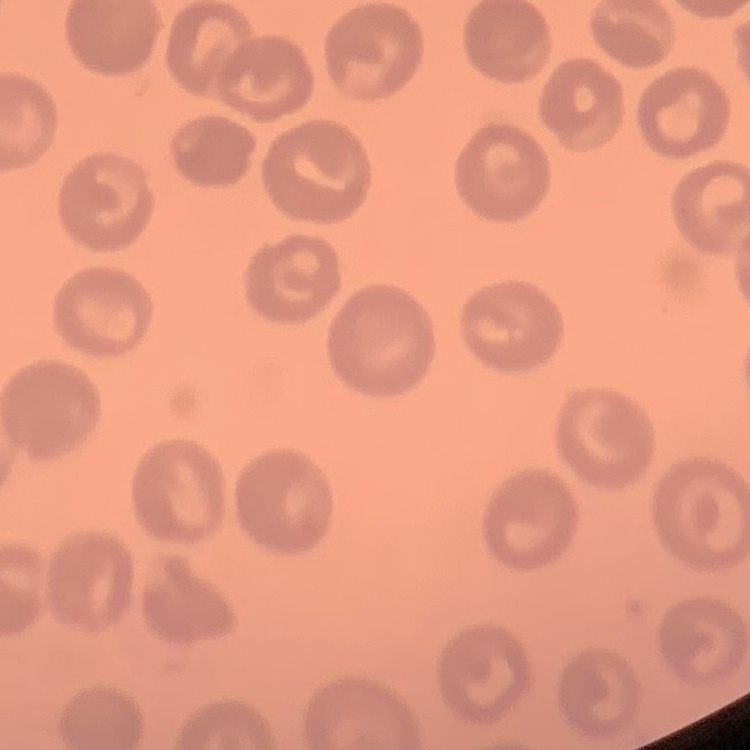
erythrocyte morphology = no rouleaux formation
preparation = thin blood smear
stain = Field's or Giemsa
image type = square crop of a larger photomicrograph